State the preparation type.
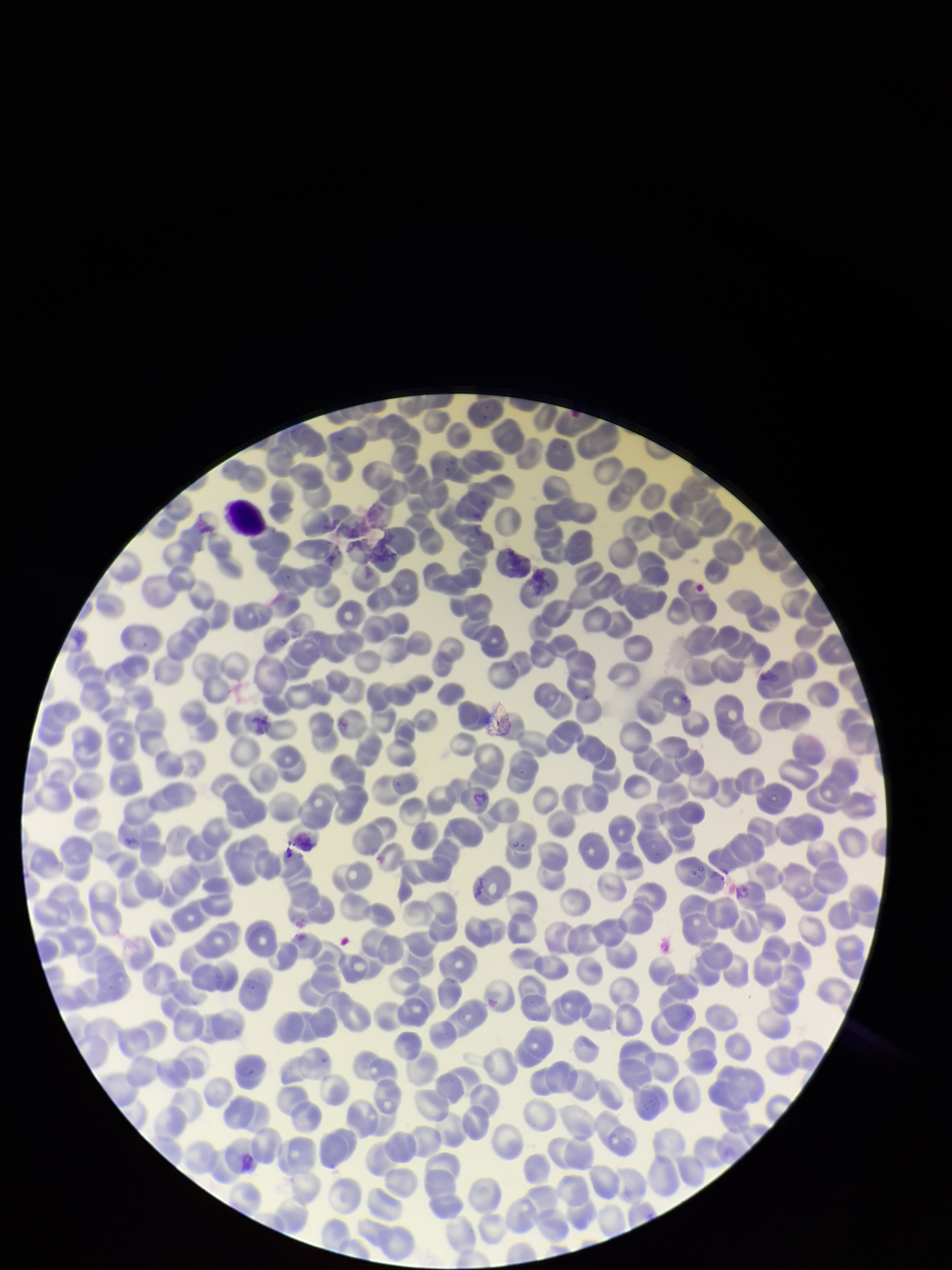

Thin.

image size = 952×1270 pixels
parasitized red blood cells = none seen
capture = smartphone photograph through the microscope eyepiece
field of view = one from this slide
parasitized red blood cell count = 0
stain = Giemsa
red blood cell count = 222
patient malaria status = negative